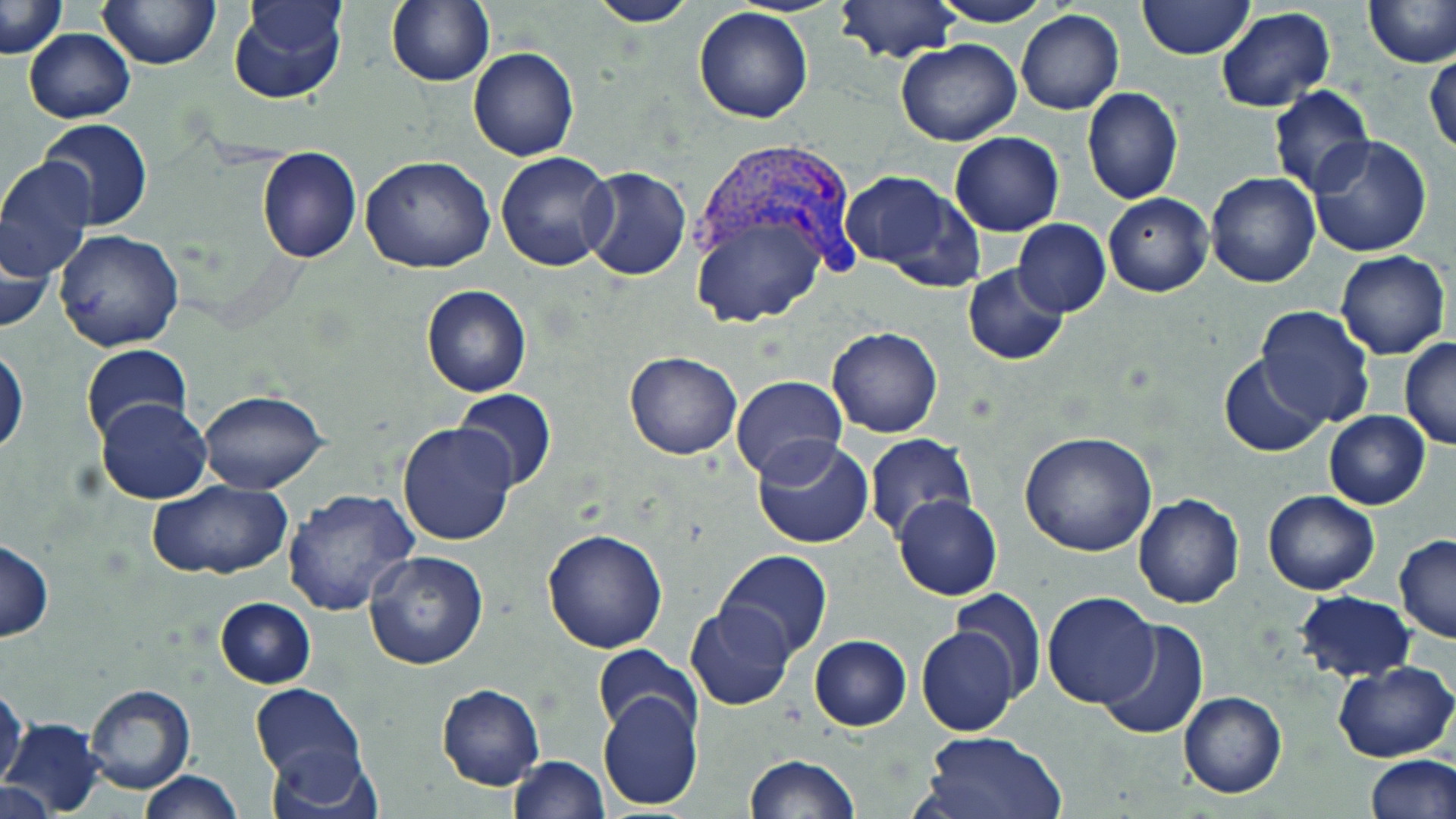

slide-level diagnosis = Plasmodium vivax
field of view = one of a larger specimen
modality = optical microscopy
image size = 1456×819 pixels
Plasmodium vivax-infected red blood cell locations = approximate bounding boxes as (x1, y1, x2, y2) in pixels: (692, 135, 863, 294)
uninfected red blood cell locations = approximate bounding boxes as (x1, y1, x2, y2) in pixels: (2, 0, 68, 58), (228, 0, 348, 106), (387, 0, 494, 87), (834, 0, 961, 63), (929, 0, 1056, 27), (1138, 0, 1254, 60), (99, 1, 220, 70), (584, 1, 700, 26), (1365, 1, 1456, 67), (1214, 6, 1337, 114), (694, 7, 815, 124), (1016, 9, 1124, 114), (24, 29, 134, 123), (896, 39, 1021, 147), (468, 47, 579, 161), (1425, 51, 1456, 158), (1267, 85, 1375, 198), (1082, 87, 1185, 204), (38, 118, 152, 233), (948, 132, 1065, 237), (1306, 136, 1433, 257), (256, 145, 362, 264), (495, 152, 618, 272), (359, 155, 496, 274), (0, 158, 97, 283), (579, 167, 692, 281), (840, 170, 977, 286), (1205, 172, 1322, 290), (1103, 192, 1214, 297), (689, 206, 830, 330), (1012, 219, 1110, 317), (1, 220, 55, 336), (54, 232, 184, 353), (1335, 251, 1450, 359), (963, 263, 1069, 366), (421, 283, 531, 398), (1254, 306, 1376, 429), (826, 326, 943, 438), (1399, 338, 1456, 451), (1, 343, 28, 456), (81, 344, 193, 442), (624, 351, 741, 459), (1219, 353, 1329, 457), (730, 376, 849, 483), (452, 388, 557, 492), (197, 390, 330, 493), (95, 396, 212, 505), (1323, 411, 1432, 510), (397, 421, 517, 546), (1019, 432, 1158, 557), (862, 433, 977, 540), (751, 436, 873, 550), (146, 480, 293, 580), (281, 489, 421, 615), (1264, 491, 1380, 594), (893, 494, 1003, 599), (1132, 494, 1245, 608), (541, 529, 668, 653), (1394, 535, 1456, 643), (0, 538, 53, 642), (365, 550, 490, 671), (715, 551, 834, 659), (950, 587, 1047, 699), (1297, 591, 1417, 683), (1042, 593, 1159, 708), (215, 597, 315, 687), (685, 605, 795, 710), (1095, 617, 1210, 742), (917, 625, 1020, 736), (809, 633, 911, 730), (592, 645, 701, 740), (1332, 660, 1454, 762), (250, 683, 365, 786), (437, 683, 545, 791), (84, 684, 195, 795), (0, 685, 26, 791), (597, 690, 702, 811), (1177, 690, 1287, 798), (1, 718, 104, 817), (914, 730, 1067, 819), (261, 741, 382, 818), (510, 755, 610, 818), (744, 755, 859, 818), (1365, 757, 1456, 818), (141, 771, 243, 819), (1, 780, 55, 818)
magnification = 1000x
stain = May-Grünwald-Giemsa
preparation = thin blood smear